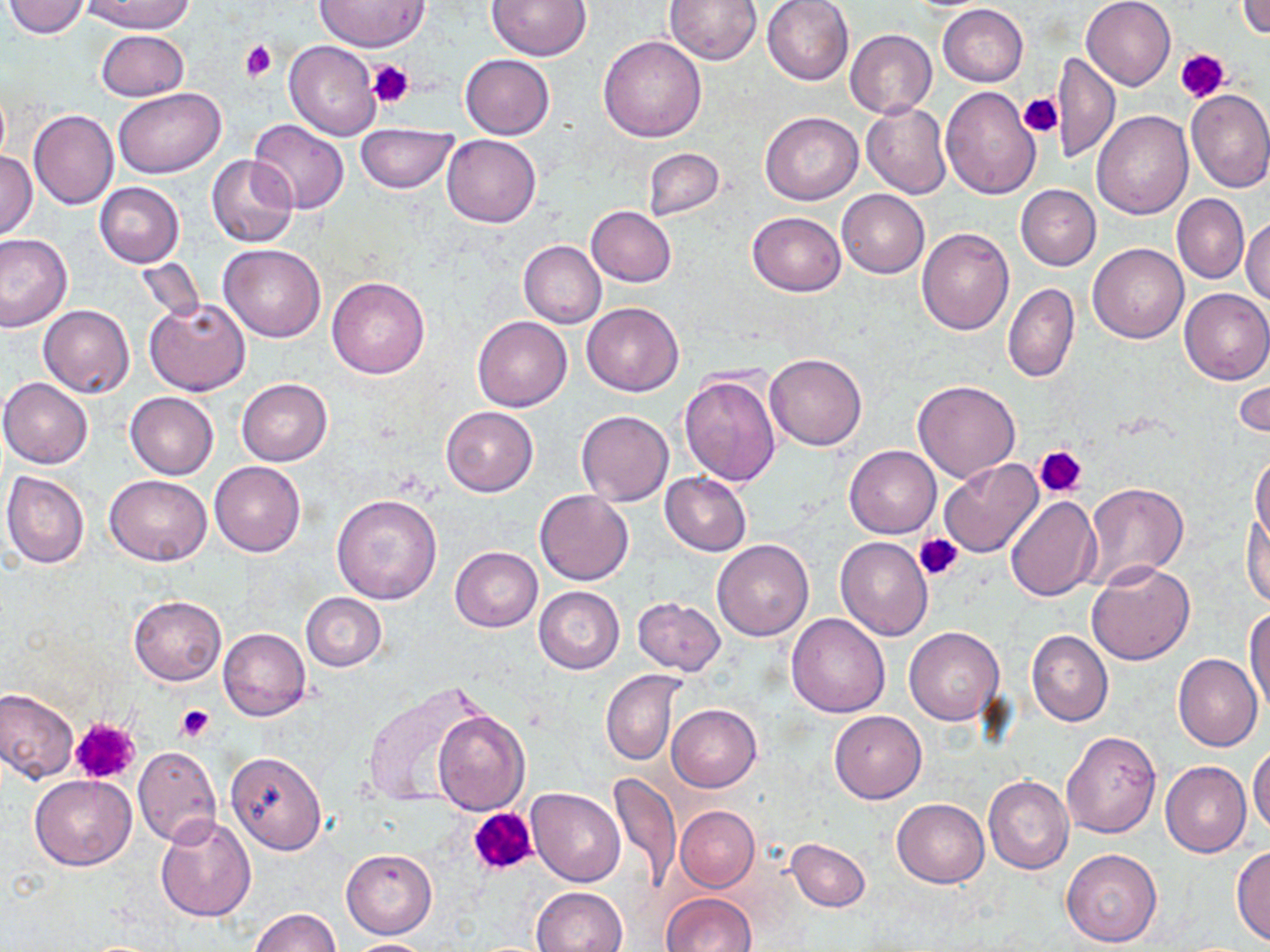
slide_level_diagnosis: no evidence of blood parasites
modality: optical microscopy
platelet_locations: 'approximate bounding boxes as (x1,y1)-(x2,y2) corner pairs in pixels: (240,41)-(277,81), (1175,47)-(1230,103), (366,60)-(415,108), (1017,93)-(1062,138), (1035,445)-(1086,499), (915,532)-(964,581), (175,705)-(215,742), (69,717)-(142,786), (468,807)-(538,877)'
image_size: 1270×952 pixels
preparation: thin blood film
field_of_view: one of a larger specimen
magnification: 1000x
stain: May-Grünwald-Giemsa
uninfected_red_blood_cell_locations: 'approximate bounding boxes as (x1,y1)-(x2,y2) corner pairs in pixels: (80,0)-(195,34), (315,0)-(426,52), (487,0)-(589,60), (664,0)-(763,64), (762,0)-(854,85), (1082,0)-(1176,89), (1236,0)-(1270,39), (4,1)-(92,38), (938,4)-(1027,86), (97,28)-(188,101), (846,30)-(937,118), (598,35)-(708,142), (284,42)-(382,141), (1051,53)-(1120,162), (461,55)-(555,139), (941,86)-(1041,199), (113,87)-(224,177), (1186,89)-(1270,194), (862,101)-(952,200), (29,110)-(119,211), (1092,110)-(1192,218), (760,112)-(863,205), (248,119)-(348,214), (355,122)-(459,192), (441,134)-(542,228), (643,148)-(725,222), (0,151)-(37,239), (207,155)-(297,248), (95,182)-(184,267), (1016,184)-(1101,270), (838,190)-(930,279), (1172,194)-(1249,283), (586,206)-(676,287), (748,211)-(846,295), (1242,216)-(1270,306), (917,228)-(1013,334), (0,233)-(72,331), (518,240)-(605,328), (1088,243)-(1189,343), (219,244)-(327,342), (136,258)-(205,323), (326,277)-(429,379), (1004,282)-(1079,382), (1179,288)-(1270,383), (145,298)-(251,395), (583,303)-(685,395), (39,304)-(135,399), (472,315)-(572,412), (765,353)-(868,450), (1232,371)-(1270,443), (679,373)-(781,486), (0,378)-(93,468), (236,378)-(332,466), (913,380)-(1021,483), (125,392)-(218,479), (441,406)-(538,496), (575,409)-(674,506), (844,446)-(941,539), (1251,454)-(1270,545), (939,459)-(1045,561), (210,461)-(305,558), (0,471)-(90,568), (659,471)-(752,556), (104,475)-(212,565), (1084,483)-(1189,588), (534,490)-(633,585), (332,493)-(443,605), (1005,494)-(1101,601), (1243,510)-(1269,610), (834,537)-(933,641), (712,539)-(813,641), (450,546)-(542,632), (1085,561)-(1195,665), (533,586)-(625,674), (300,592)-(386,671), (129,595)-(226,685), (632,596)-(725,674), (1246,606)-(1270,718), (786,614)-(890,717), (218,627)-(310,721), (905,627)-(1004,726), (1027,630)-(1113,727), (1173,654)-(1263,753), (601,671)-(682,766), (361,681)-(491,805), (1,687)-(79,782), (667,704)-(761,791), (433,708)-(530,814), (829,711)-(926,803), (1061,729)-(1159,838), (1249,744)-(1270,834), (133,746)-(221,846), (225,750)-(327,854), (1161,761)-(1251,857), (610,772)-(682,889), (29,774)-(136,869), (983,776)-(1073,875), (526,787)-(625,886), (892,797)-(989,887), (675,806)-(759,890), (153,814)-(257,922), (787,838)-(870,911), (1231,847)-(1270,946), (341,849)-(437,938), (1062,849)-(1162,947), (531,886)-(629,952), (662,892)-(757,952), (249,908)-(340,952), (340,938)-(440,951)'